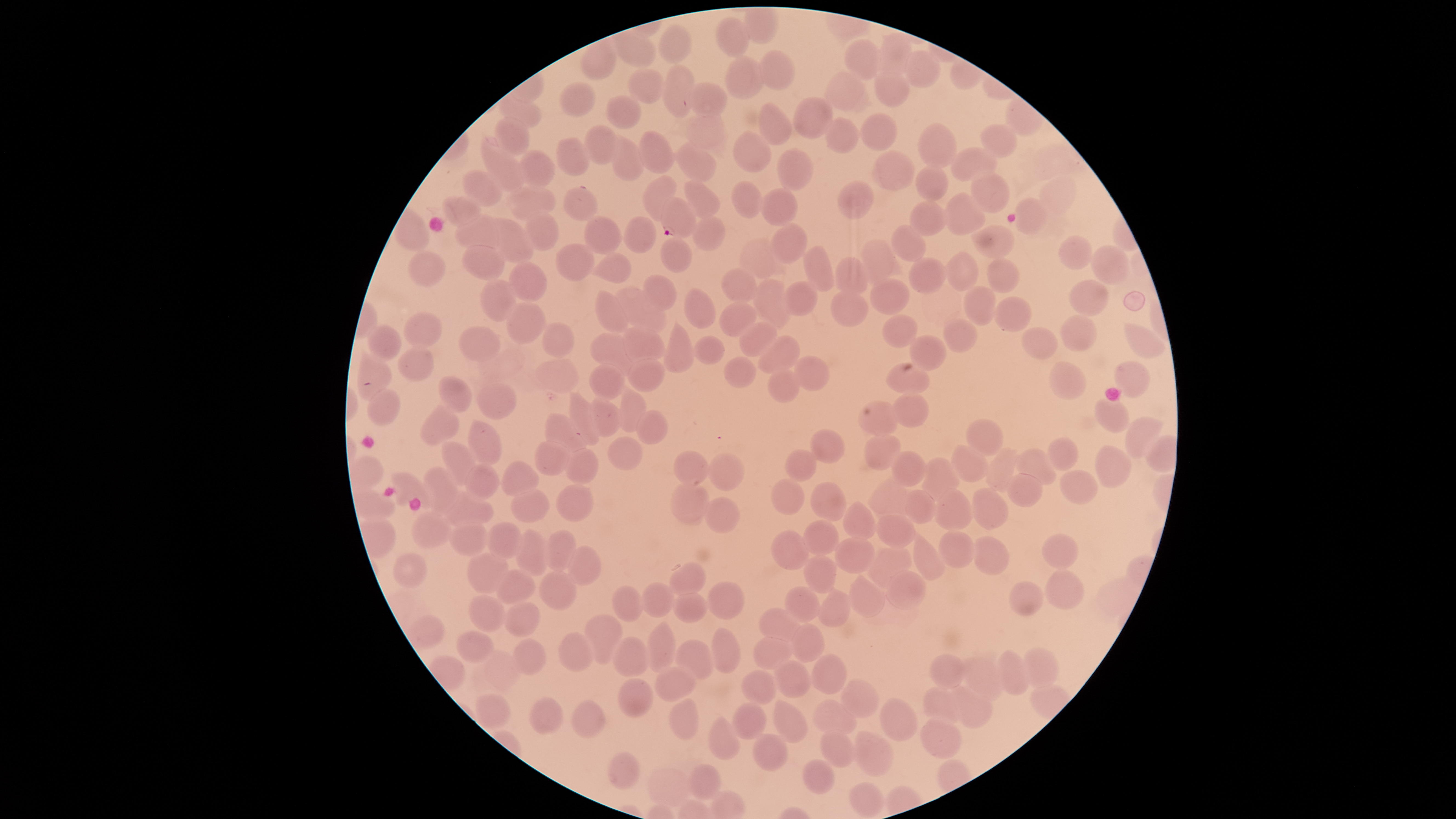 Approximate bounding boxes as (left, top, right, bottom) in pixels. Parasitized red blood cells: (661, 196, 697, 238). Uninfected red blood cells: (716, 17, 750, 57), (658, 24, 693, 63), (876, 34, 912, 75), (845, 40, 882, 80), (759, 50, 796, 91), (903, 50, 942, 89), (725, 56, 765, 99), (662, 64, 694, 118), (874, 67, 909, 107), (626, 68, 668, 104), (824, 72, 865, 112), (559, 81, 595, 117), (689, 83, 728, 117), (605, 96, 640, 129), (793, 98, 833, 138), (759, 103, 791, 146), (686, 112, 724, 149), (859, 114, 897, 150), (494, 117, 529, 156), (824, 117, 859, 153), (917, 122, 957, 168), (980, 124, 1018, 158), (584, 125, 619, 165), (639, 130, 675, 173), (733, 131, 771, 172), (480, 135, 526, 193), (610, 136, 645, 180), (556, 137, 589, 177), (677, 142, 716, 182), (777, 147, 813, 191), (951, 147, 997, 183), (872, 149, 915, 190), (519, 150, 555, 187), (915, 166, 947, 202), (461, 169, 503, 207), (970, 172, 1009, 214), (642, 175, 677, 220), (1039, 177, 1078, 215), (685, 178, 720, 220), (731, 180, 762, 219), (837, 180, 873, 220), (506, 184, 556, 220), (563, 185, 597, 221), (760, 188, 798, 227), (944, 193, 985, 236), (442, 196, 483, 227), (1014, 198, 1048, 236), (910, 199, 948, 237), (525, 211, 558, 251), (455, 214, 499, 254), (692, 214, 725, 252), (624, 215, 656, 254), (485, 217, 535, 263), (583, 217, 622, 255), (769, 223, 808, 264), (972, 223, 1014, 259), (890, 225, 926, 262), (660, 235, 692, 273), (1059, 236, 1093, 270), (861, 239, 895, 286), (740, 240, 775, 279), (556, 244, 595, 282), (462, 245, 506, 281), (1090, 245, 1129, 285), (801, 246, 833, 292), (407, 250, 445, 287), (593, 252, 631, 284), (946, 252, 979, 292), (833, 258, 868, 296), (909, 258, 945, 295), (986, 258, 1019, 293), (509, 262, 546, 302), (721, 267, 757, 303), (643, 275, 677, 310), (870, 278, 910, 315), (480, 279, 517, 322), (1069, 279, 1109, 317), (751, 280, 791, 328), (782, 282, 817, 316), (962, 284, 996, 326), (614, 288, 666, 334), (684, 288, 716, 330), (830, 289, 868, 327), (595, 290, 629, 333), (993, 297, 1031, 333), (507, 301, 547, 345), (720, 302, 756, 337), (403, 312, 442, 349), (1060, 313, 1097, 352), (882, 315, 918, 349), (739, 317, 776, 358), (942, 317, 977, 353), (542, 322, 574, 359), (657, 322, 692, 374), (623, 323, 666, 364), (1124, 323, 1163, 358), (368, 324, 401, 363), (1022, 326, 1059, 359), (458, 327, 501, 362), (591, 332, 637, 376), (694, 334, 725, 366), (909, 335, 947, 371), (756, 336, 800, 374), (397, 347, 434, 382), (357, 354, 393, 401), (724, 356, 756, 388), (792, 356, 831, 392), (627, 358, 664, 394), (536, 360, 579, 395), (886, 362, 930, 395), (1049, 362, 1086, 400), (1114, 362, 1151, 398), (588, 365, 625, 401), (769, 369, 800, 403), (439, 376, 471, 413), (477, 384, 518, 421), (367, 389, 400, 427), (619, 389, 647, 433), (568, 392, 600, 445), (892, 393, 929, 427), (589, 398, 621, 437), (1095, 399, 1131, 433), (858, 400, 898, 437), (420, 406, 461, 446), (636, 409, 668, 444), (545, 412, 587, 455), (1125, 417, 1165, 460), (965, 418, 1004, 457), (468, 420, 501, 464), (809, 429, 844, 464), (864, 433, 900, 471), (608, 435, 642, 471), (1047, 436, 1078, 471), (442, 440, 476, 486), (534, 440, 571, 476), (951, 443, 988, 483), (1095, 445, 1132, 489), (1017, 447, 1057, 486), (564, 448, 598, 485), (985, 448, 1020, 493), (673, 449, 709, 486), (786, 449, 816, 483), (889, 451, 926, 487), (708, 453, 744, 491), (349, 456, 384, 490), (921, 457, 959, 500), (501, 460, 539, 497), (464, 462, 499, 500), (423, 467, 460, 508), (1060, 468, 1098, 505), (390, 471, 434, 509), (1007, 472, 1043, 507), (868, 477, 909, 515), (770, 478, 804, 517), (671, 482, 710, 523), (809, 482, 846, 522), (555, 483, 593, 522), (972, 486, 1008, 530), (933, 488, 973, 531), (509, 489, 550, 522), (900, 489, 937, 524), (440, 491, 494, 527), (704, 497, 742, 533), (843, 501, 876, 540), (412, 512, 452, 548), (875, 514, 915, 549), (801, 519, 839, 555), (449, 522, 488, 557), (486, 523, 522, 560), (771, 529, 809, 570), (515, 530, 548, 576), (545, 530, 576, 572), (938, 530, 975, 568), (1042, 534, 1078, 569), (834, 536, 875, 573), (912, 536, 945, 581), (970, 536, 1011, 575), (566, 546, 601, 585), (867, 546, 911, 590), (394, 553, 427, 588), (466, 553, 508, 594), (803, 555, 836, 594), (669, 562, 706, 596), (495, 570, 535, 604), (884, 570, 926, 610), (1044, 570, 1085, 610), (539, 571, 577, 612), (849, 576, 885, 617), (707, 580, 744, 620), (1008, 580, 1043, 616), (640, 582, 674, 618), (611, 586, 644, 623), (784, 586, 821, 622), (818, 589, 851, 627), (673, 592, 709, 624), (468, 594, 506, 633), (503, 602, 540, 637), (758, 607, 802, 643), (583, 614, 622, 665), (789, 623, 825, 662), (645, 624, 676, 675), (711, 626, 740, 674), (454, 630, 496, 664), (557, 632, 595, 672), (612, 636, 648, 678), (753, 636, 793, 671), (511, 638, 546, 675), (676, 639, 715, 680), (1020, 648, 1059, 687), (471, 649, 520, 696), (996, 650, 1030, 695), (812, 653, 847, 694), (929, 653, 966, 691), (957, 656, 1003, 702), (773, 660, 810, 698), (654, 666, 695, 702), (741, 669, 777, 706), (617, 678, 653, 718), (840, 679, 880, 718), (923, 686, 961, 730), (950, 686, 991, 729), (475, 693, 510, 729), (529, 697, 562, 734), (880, 697, 916, 742), (668, 698, 697, 741), (570, 699, 605, 738), (812, 699, 855, 736), (772, 700, 807, 744), (732, 702, 767, 739), (708, 717, 739, 759), (920, 719, 961, 759), (820, 730, 855, 768), (855, 730, 893, 776), (752, 733, 787, 770), (608, 751, 639, 790), (802, 759, 834, 794), (689, 764, 721, 800), (646, 768, 690, 807), (848, 782, 882, 817). Image is 1456×819 pixels. Giemsa-stained preparation. Presence: malaria parasites detected. Thin smear of blood. Species: Plasmodium falciparum. The visible region is circular. One field of view of the specimen. Smartphone photograph through the microscope eyepiece.